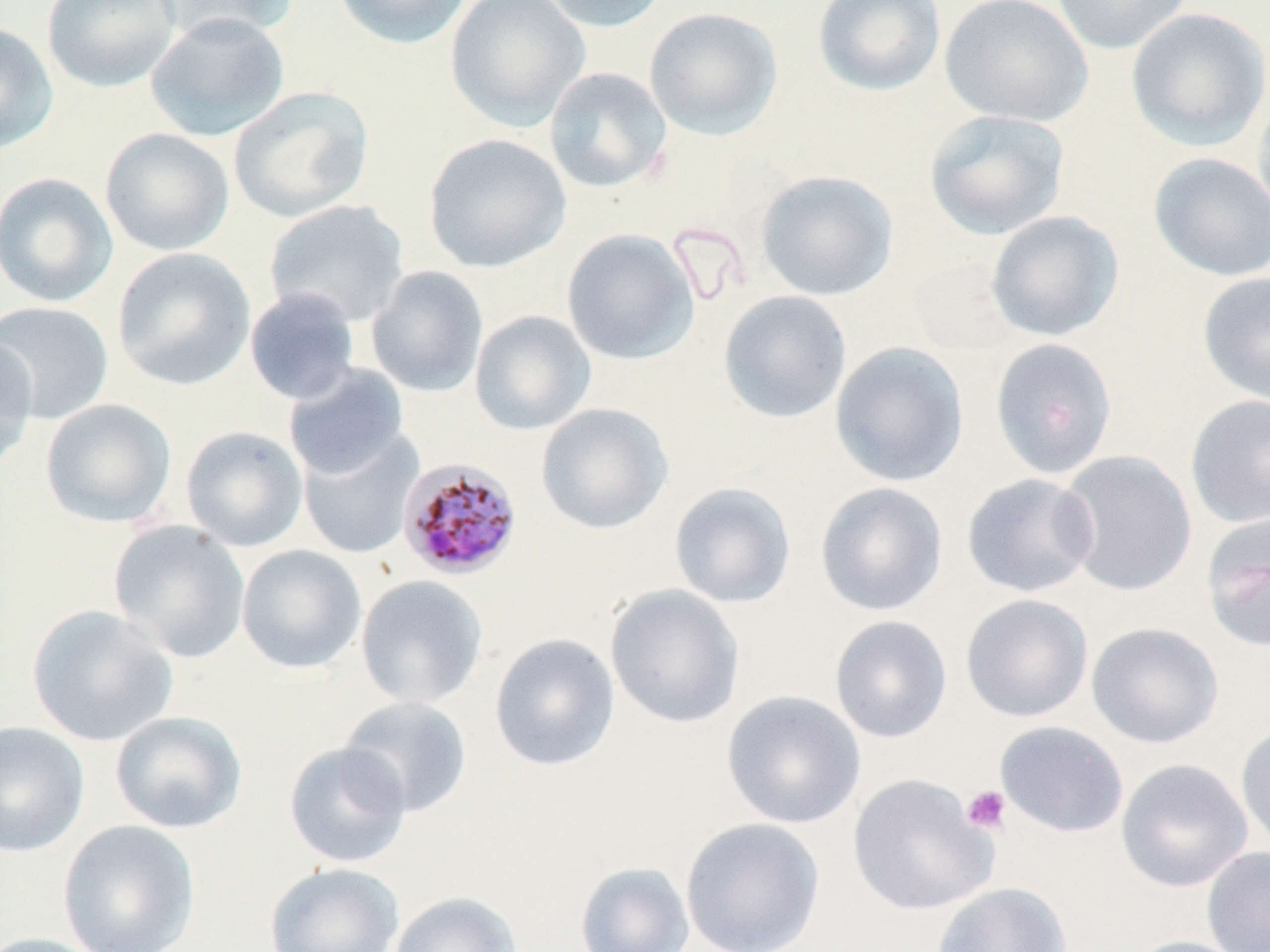 Approximate bounding boxes as (x1,y1)-(x2,y2) corner pairs in pixels. Plasmodium malariae-infected red blood cell locations: (397,457)-(523,580). Platelet locations: (960,784)-(1011,835). Uninfected red blood cell locations: (40,0)-(181,93), (150,0)-(296,46), (333,0)-(473,49), (444,0)-(590,131), (535,0)-(670,34), (812,0)-(946,96), (938,0)-(1093,127), (1050,0)-(1193,56), (643,6)-(784,141), (1126,7)-(1270,152), (144,11)-(291,141), (0,21)-(59,155), (543,66)-(672,193), (228,85)-(375,223), (1252,87)-(1270,234), (923,109)-(1071,241), (99,127)-(235,257), (423,133)-(572,272), (1148,152)-(1270,283), (755,170)-(900,301), (0,172)-(119,308), (264,199)-(410,328), (986,211)-(1124,342), (561,229)-(701,365), (111,247)-(256,391), (905,256)-(1022,356), (365,265)-(488,397), (1197,272)-(1270,406), (244,287)-(361,406), (718,290)-(852,424), (0,300)-(114,424), (470,310)-(597,435), (0,333)-(38,471), (990,338)-(1118,479), (830,342)-(970,487), (283,364)-(410,480), (1185,394)-(1270,529), (39,398)-(177,529), (536,403)-(674,535), (180,425)-(308,552), (297,426)-(423,560), (1056,450)-(1198,596), (961,473)-(1100,598), (669,482)-(797,609), (814,482)-(949,616), (1201,512)-(1270,653), (108,520)-(251,663), (236,544)-(367,674), (355,574)-(488,709), (605,584)-(745,730), (960,593)-(1094,723), (26,605)-(178,748), (829,615)-(953,743), (1086,621)-(1225,749), (489,633)-(621,772), (721,690)-(866,829), (337,696)-(472,818), (109,711)-(247,834), (0,721)-(90,857), (994,721)-(1129,839), (1235,721)-(1270,857), (283,742)-(412,868), (1115,758)-(1254,892), (847,774)-(999,916), (680,817)-(825,952), (57,819)-(201,952), (1201,846)-(1270,952), (264,861)-(405,952), (574,861)-(695,952), (931,882)-(1073,952), (387,891)-(523,952), (0,933)-(110,952), (1122,935)-(1256,952). Slide-level diagnosis: Plasmodium malariae. Image is 1270×952 pixels. One field of a larger specimen. Light microscopy. 1000x magnification. Thin blood film. May-Grünwald-Giemsa-stained preparation.